Classify this cell by malaria status.
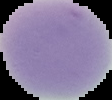

Uninfected.

Summary:
  - Image type: segmented cell region with the area outside set to black
  - Preparation: thin blood film
  - Image size: 112×100 pixels